Classify this cell by malaria status.
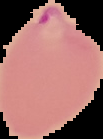
It is parasitized.

image size = 103×139 pixels
preparation = thin blood smear
image type = segmented cell region on a black background